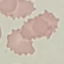
Malaria status: uninfected. Acquired by smartphone through the microscope eyepiece. Giemsa stain. Thin smear of blood. Automatically extracted cell patch, resized to 64 × 64 pixels.